Locate every P. falciparum parasite and give its life-cycle stage, and locate every leukocyte and any debris.
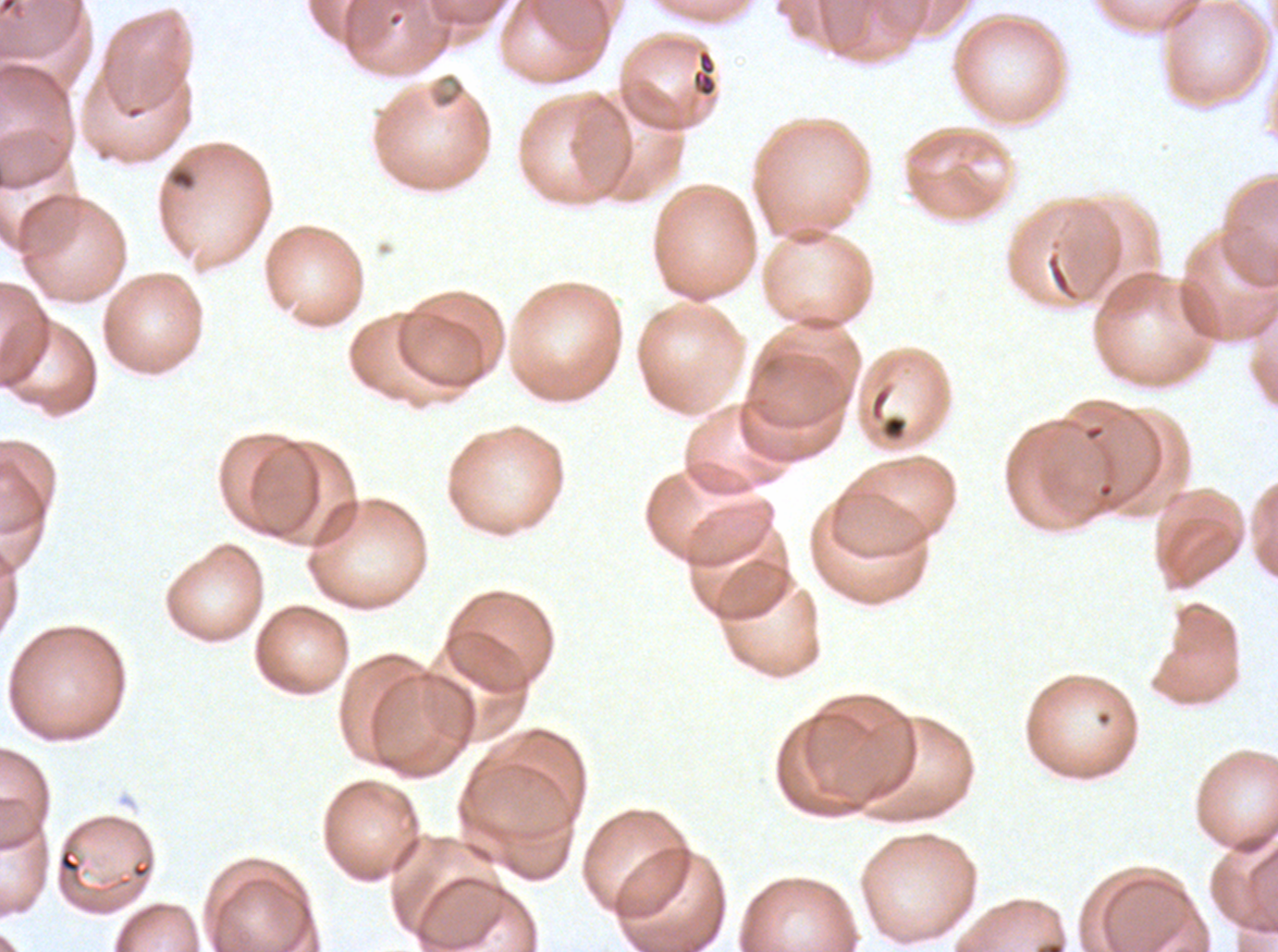
Approximate bounding boxes as {x1, y1, x2, y2} in pixels.
Debris: {691, 48, 719, 98}, {428, 71, 467, 110}, {168, 165, 197, 191}, {869, 383, 909, 444}.
No rings, late-ring/early-trophozoite forms, mid trophozoites, late trophozoites, early schizonts, late schizonts, segmenters, gametocytes, or leukocytes observed.

Summary:
  - Specimen: P. falciparum cultured ex vivo for 24 to 48 hours, from a patient in The Gambia
  - Field of view: one sub-image of a larger composite
  - Stain: Giemsa
  - Image size: 1278×952 pixels
  - Preparation: thin blood film